Classify this cell by malaria status.
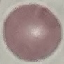
Uninfected.

Cell patch, automatically extracted from a larger field of view and resized to 64 × 64 pixels. Giemsa-stained preparation. Photographed with a smartphone camera at the microscope eyepiece. Thin blood smear.